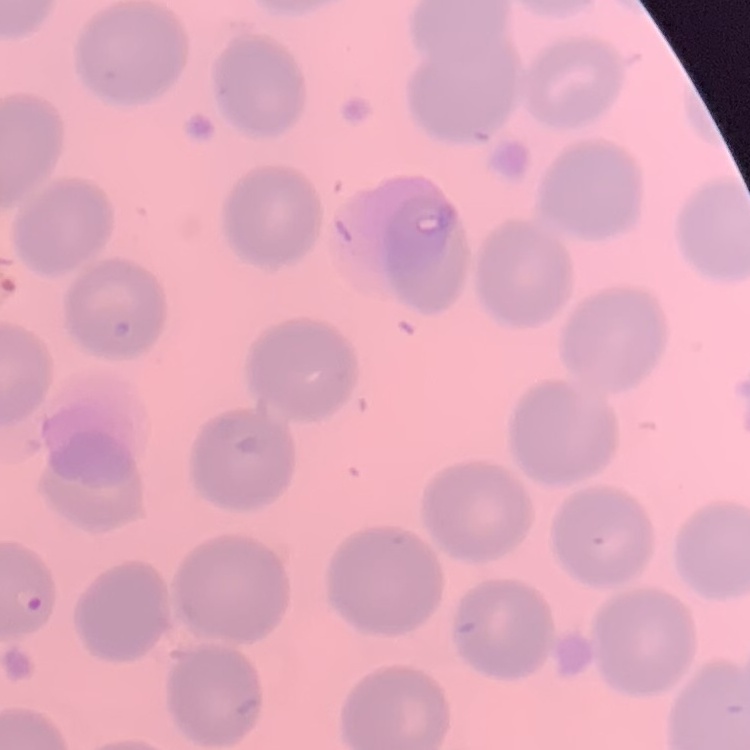
The red blood cells exhibit no rouleaux formation. Thin blood smear. One tile cut from a larger photomicrograph. Field's or Giemsa stain.